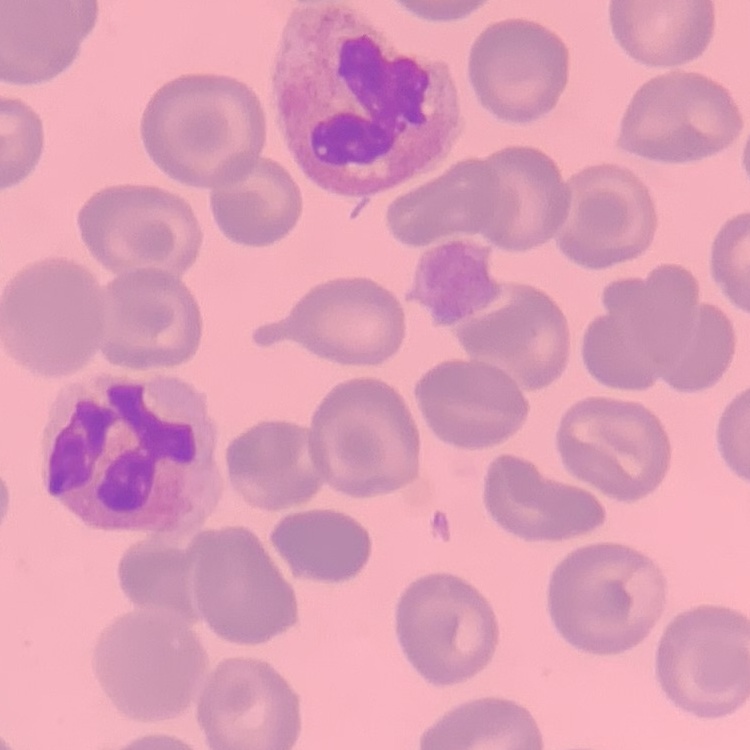

red blood cell morphology = no rouleaux formation
image type = one tile cut from a larger photomicrograph
stain = Field's or Giemsa
preparation = thin blood film